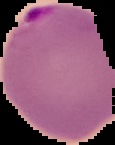 Malaria status: parasitized. From a thin blood film. Segmented cell region on a black background. Image is 115×145 pixels.